State the blood parasite species.
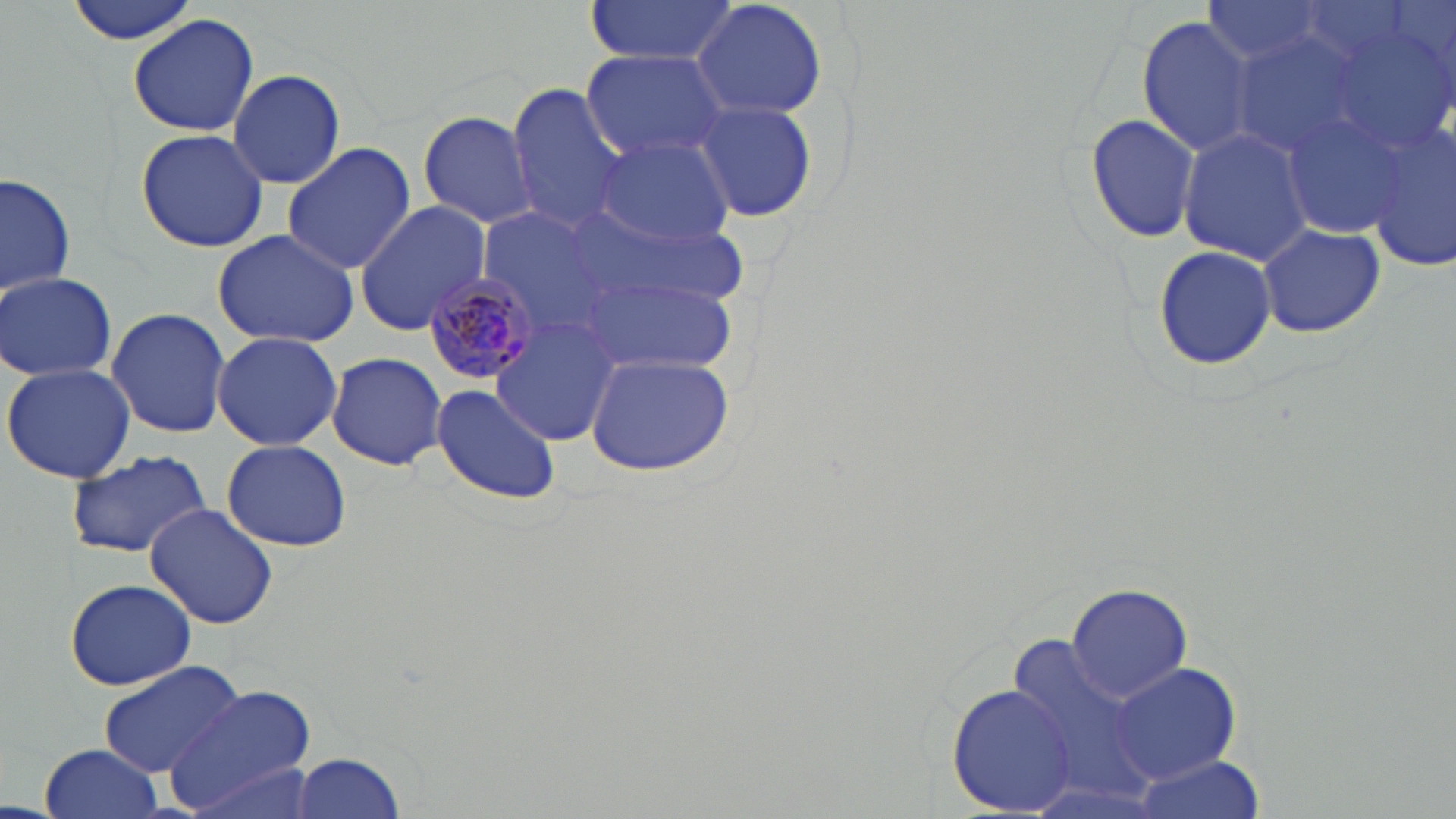
Plasmodium malariae.

Summary:
  - Coordinate format: approximate bounding boxes as (x1,y1)-(x2,y2) corner pairs in pixels
  - Plasmodium malariae-infected red blood cell locations: (423,272)-(544,384)
  - Uninfected red blood cell locations: (64,0)-(201,45), (692,0)-(829,122), (582,1)-(740,66), (127,13)-(259,137), (1137,16)-(1255,155), (1117,30)-(1237,234), (1231,32)-(1373,159), (581,49)-(731,165), (228,66)-(346,189), (506,82)-(629,231), (692,99)-(819,223), (1274,99)-(1410,246), (416,110)-(540,229), (1083,112)-(1201,246), (1364,120)-(1456,272), (1179,129)-(1316,265), (135,130)-(270,254), (594,137)-(737,248), (282,142)-(415,276), (2,173)-(77,300), (353,200)-(491,334), (575,205)-(743,311), (1254,222)-(1385,339), (213,227)-(361,351), (1150,242)-(1278,373), (581,270)-(737,375), (0,271)-(119,382), (107,307)-(230,438), (493,319)-(622,443), (212,331)-(342,451), (446,345)-(597,480), (326,351)-(448,471), (583,351)-(737,476), (1,361)-(136,484), (430,384)-(561,505), (222,438)-(352,553), (65,449)-(213,558), (145,501)-(278,629), (64,577)-(197,691), (1066,583)-(1193,701), (992,628)-(1176,809), (96,660)-(247,780), (1108,662)-(1243,786), (946,684)-(1077,813), (167,685)-(322,817), (39,742)-(165,819), (292,753)-(407,819), (1125,755)-(1264,819)
  - Preparation: thin blood film
  - Field of view: one of a larger specimen
  - Magnification: 1000x
  - Image size: 1456×819 pixels
  - Modality: optical microscopy
  - Stain: May-Grünwald-Giemsa